Identify the blood parasite species.
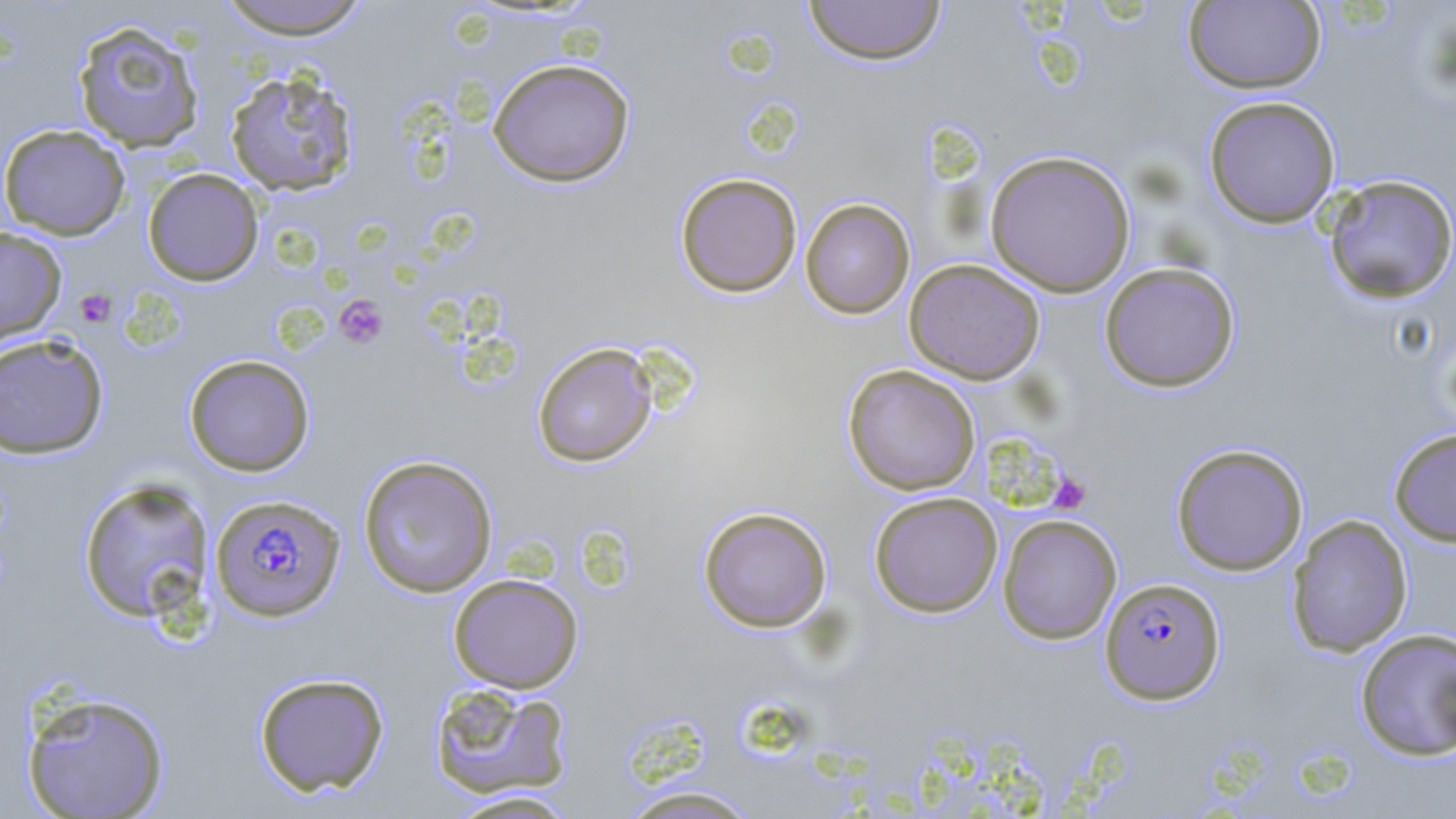

Plasmodium falciparum.

{
  "preparation": "thin blood film",
  "platelet_locations": "approximate bounding boxes as named x1/y1/x2/y2 corners in pixels: (x1=74, y1=288, x2=116, y2=328), (x1=334, y1=295, x2=390, y2=350), (x1=1049, y1=473, x2=1091, y2=514)",
  "field_of_view": "single",
  "modality": "light microscopy",
  "magnification": "1000x",
  "plasmodium_falciparum_infected_red_blood_cell_locations": "approximate bounding boxes as named x1/y1/x2/y2 corners in pixels: (x1=210, y1=493, x2=347, y2=622), (x1=1100, y1=577, x2=1225, y2=704)",
  "uninfected_red_blood_cell_locations": "approximate bounding boxes as named x1/y1/x2/y2 corners in pixels: (x1=215, y1=0, x2=374, y2=39), (x1=1183, y1=0, x2=1326, y2=94), (x1=803, y1=1, x2=947, y2=66), (x1=72, y1=19, x2=206, y2=152), (x1=487, y1=58, x2=636, y2=187), (x1=224, y1=67, x2=360, y2=197), (x1=1203, y1=95, x2=1341, y2=228), (x1=0, y1=123, x2=131, y2=239), (x1=984, y1=149, x2=1137, y2=297), (x1=143, y1=168, x2=264, y2=286), (x1=675, y1=172, x2=803, y2=298), (x1=1323, y1=174, x2=1456, y2=303), (x1=800, y1=197, x2=915, y2=318), (x1=0, y1=226, x2=66, y2=346), (x1=904, y1=259, x2=1045, y2=384), (x1=1099, y1=262, x2=1241, y2=392), (x1=0, y1=333, x2=109, y2=459), (x1=531, y1=342, x2=658, y2=467), (x1=183, y1=354, x2=316, y2=476), (x1=842, y1=364, x2=981, y2=495), (x1=1388, y1=427, x2=1456, y2=547), (x1=1170, y1=443, x2=1309, y2=576), (x1=358, y1=454, x2=498, y2=598), (x1=78, y1=477, x2=215, y2=623), (x1=868, y1=491, x2=1003, y2=618), (x1=697, y1=506, x2=832, y2=633), (x1=998, y1=514, x2=1122, y2=644), (x1=1287, y1=514, x2=1413, y2=657), (x1=448, y1=573, x2=583, y2=693), (x1=1354, y1=627, x2=1456, y2=761), (x1=253, y1=671, x2=390, y2=797), (x1=428, y1=682, x2=575, y2=800), (x1=20, y1=690, x2=171, y2=818), (x1=614, y1=784, x2=765, y2=818), (x1=445, y1=790, x2=581, y2=818)",
  "image_size": "1456×819 pixels",
  "stain": "May-Grünwald-Giemsa"
}